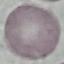
malaria_status: uninfected
image_type: cell patch, automatically extracted from a larger field of view and resized to 64 × 64 pixels
preparation: thin blood smear
stain: Giemsa
capture: smartphone through the microscope eyepiece